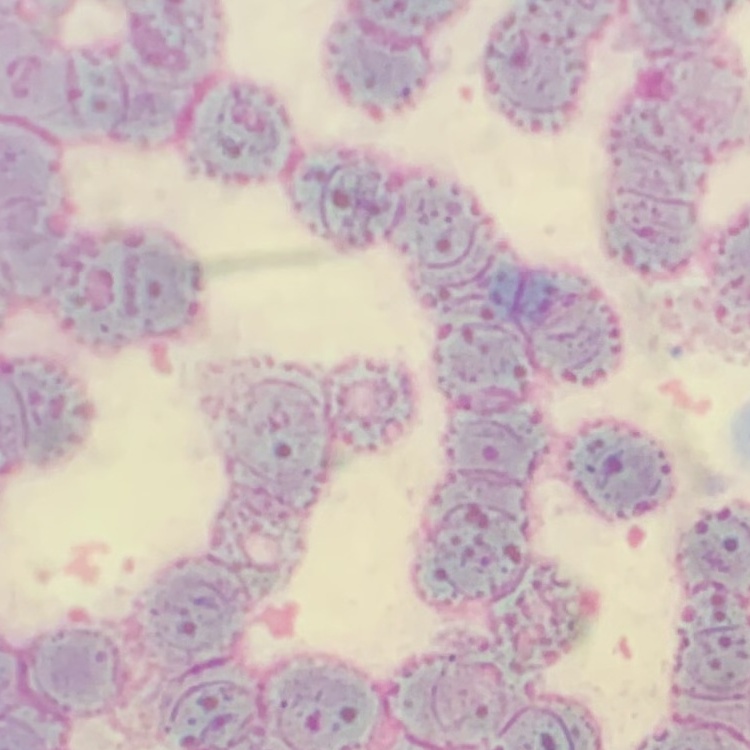
{
  "red_blood_cell_morphology": "rouleaux formation",
  "preparation": "thin blood smear",
  "image_type": "one tile cut from a larger photomicrograph",
  "stain": "Field's or Giemsa"
}